Give the position of every Plasmodium parasite visible.
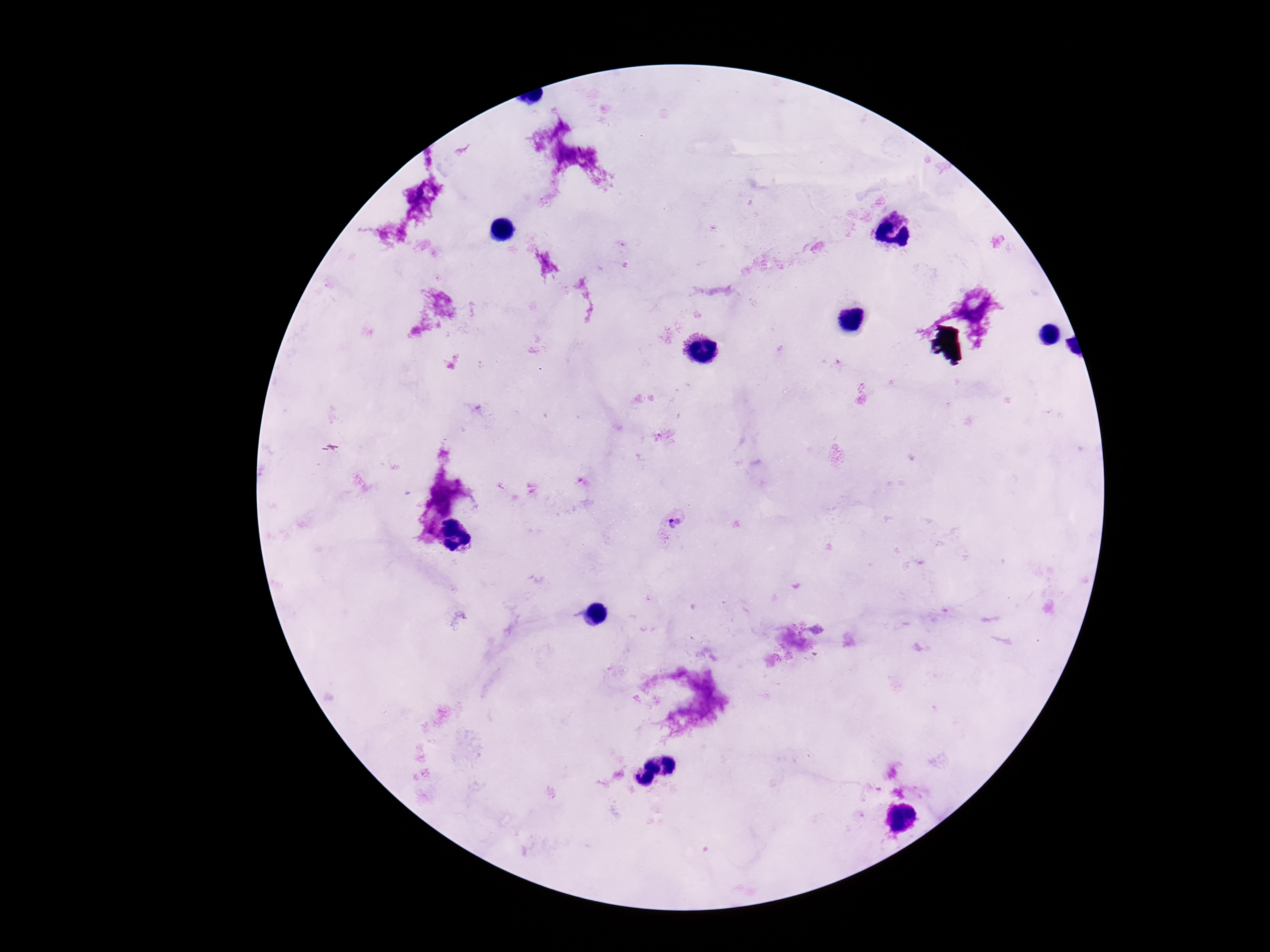

Approximate object centers, in pixels from the top-left corner.
Plasmodium parasites: (x=674, y=524).

field_of_view: one from this slide
magnification: 100x
stain: Giemsa
patient_malaria_status: positive
preparation: thick blood film
capture: smartphone camera through the microscope eyepiece
image_size: 1270×952 pixels